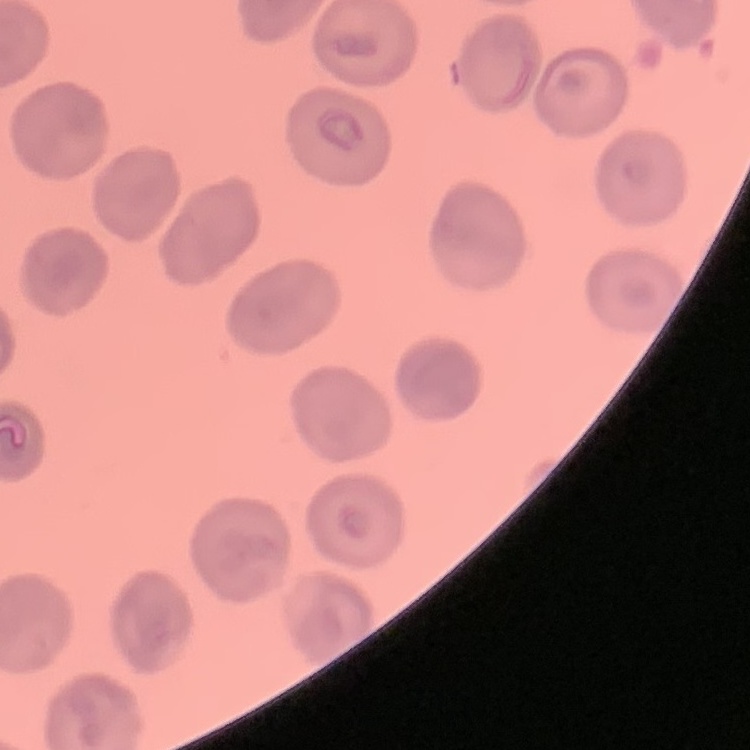 The red blood cells exhibit no rouleaux formation. Field's or Giemsa stain. Square crop of a larger photomicrograph. Thin peripheral smear.